Locate every blood parasite and identify its species.
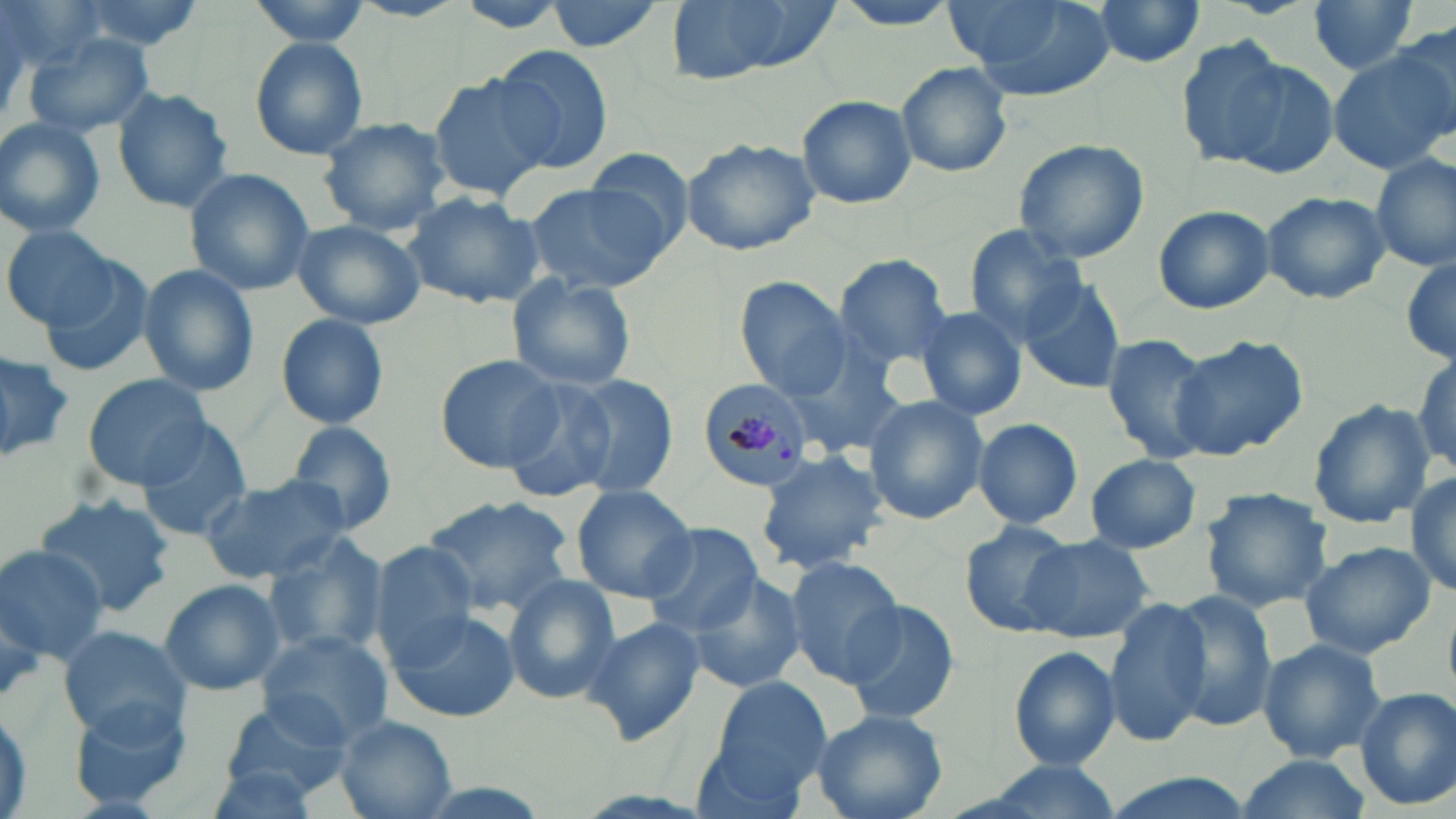
Approximate bounding boxes as [x1, y1, x2, y2] in pixels.
Plasmodium malariae-infected red blood cells: [699, 377, 818, 492].
No Plasmodium falciparum, Plasmodium ovale, Plasmodium vivax, Babesia divergens, or Trypanosoma brucei observed.

Uninfected red blood cell locations: [61, 0, 208, 56], [244, 0, 374, 48], [350, 0, 466, 22], [452, 0, 576, 34], [542, 0, 667, 54], [660, 0, 841, 86], [824, 0, 966, 34], [948, 0, 1115, 102], [1088, 0, 1208, 70], [1306, 1, 1423, 78], [24, 35, 153, 139], [248, 36, 370, 160], [1175, 38, 1325, 175], [1326, 42, 1456, 174], [495, 45, 616, 174], [895, 61, 1013, 178], [427, 71, 556, 202], [111, 86, 235, 213], [796, 96, 916, 210], [317, 116, 453, 235], [0, 118, 108, 238], [679, 135, 823, 255], [1012, 138, 1150, 262], [578, 144, 694, 248], [1372, 151, 1455, 273], [185, 168, 315, 295], [523, 180, 669, 294], [161, 182, 299, 370], [1261, 191, 1391, 306], [404, 192, 545, 308], [1152, 205, 1276, 314], [293, 220, 426, 328], [3, 222, 120, 330], [965, 224, 1089, 344], [1400, 253, 1456, 367], [835, 254, 955, 369], [40, 256, 158, 377], [136, 264, 260, 396], [506, 273, 638, 391], [734, 276, 851, 402], [1017, 278, 1127, 396], [912, 306, 1029, 421], [276, 313, 390, 429], [1098, 334, 1220, 462], [1171, 334, 1310, 458], [790, 345, 909, 455], [0, 350, 75, 464], [435, 353, 565, 472], [1412, 354, 1455, 472], [83, 374, 214, 490], [564, 374, 680, 498], [498, 379, 624, 504], [863, 395, 989, 524], [1307, 400, 1435, 528], [972, 417, 1083, 530], [283, 420, 400, 535], [133, 421, 255, 539], [754, 451, 887, 573], [1084, 453, 1202, 552], [1407, 466, 1456, 600], [199, 476, 353, 583], [570, 483, 698, 602], [1200, 487, 1333, 611], [422, 494, 577, 615], [36, 497, 173, 618], [956, 521, 1074, 636], [640, 523, 763, 637], [261, 530, 390, 657], [1020, 536, 1153, 643], [1299, 541, 1435, 659], [0, 544, 108, 663], [369, 545, 482, 667], [784, 556, 907, 684], [683, 575, 806, 695], [502, 576, 620, 704], [157, 578, 288, 696], [1164, 591, 1278, 730], [1101, 598, 1211, 747], [841, 600, 959, 727], [388, 609, 519, 723], [581, 616, 706, 746], [56, 623, 187, 741], [257, 629, 396, 748], [1257, 638, 1386, 763], [1008, 646, 1122, 770], [711, 674, 832, 789], [1354, 688, 1456, 810], [215, 699, 351, 805], [68, 700, 195, 813], [808, 707, 948, 819], [334, 714, 456, 818], [690, 738, 816, 819], [1235, 754, 1372, 819], [958, 759, 1128, 819], [200, 761, 329, 818], [1092, 771, 1261, 819]. Slide-level diagnosis: Plasmodium malariae. Thin blood smear. May-Grünwald-Giemsa-stained preparation. One field of a larger specimen. Image is 1456×819 pixels. 1000x magnification. Light microscopy.